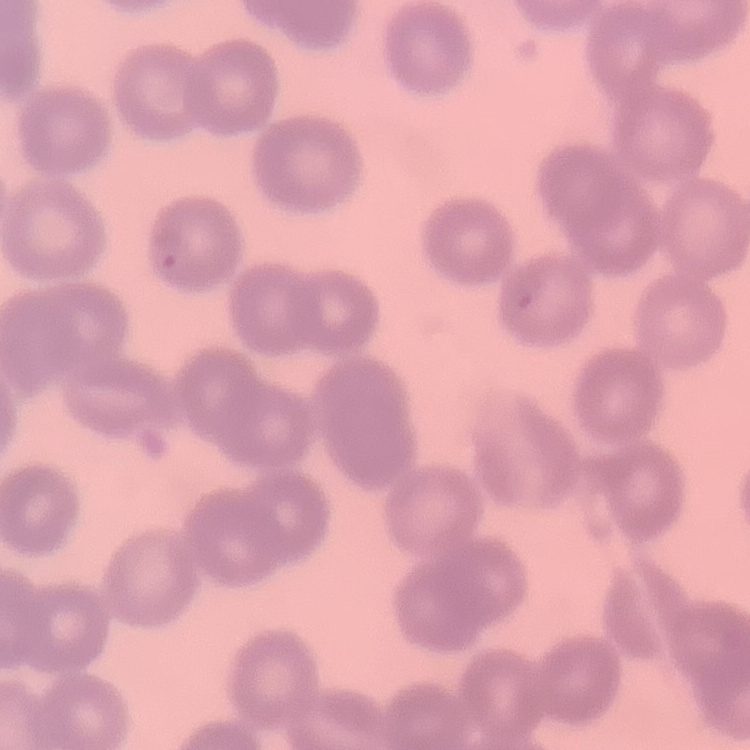
erythrocyte morphology = no rouleaux formation
stain = Field's or Giemsa
preparation = thin blood film
image type = one tile cut from a larger photomicrograph